Report the malaria status of this cell.
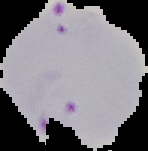
It is parasitized.

Image is 148×151 pixels. From a thin blood smear. Segmented cell region on a black background.